Describe the morphology of the erythrocytes.
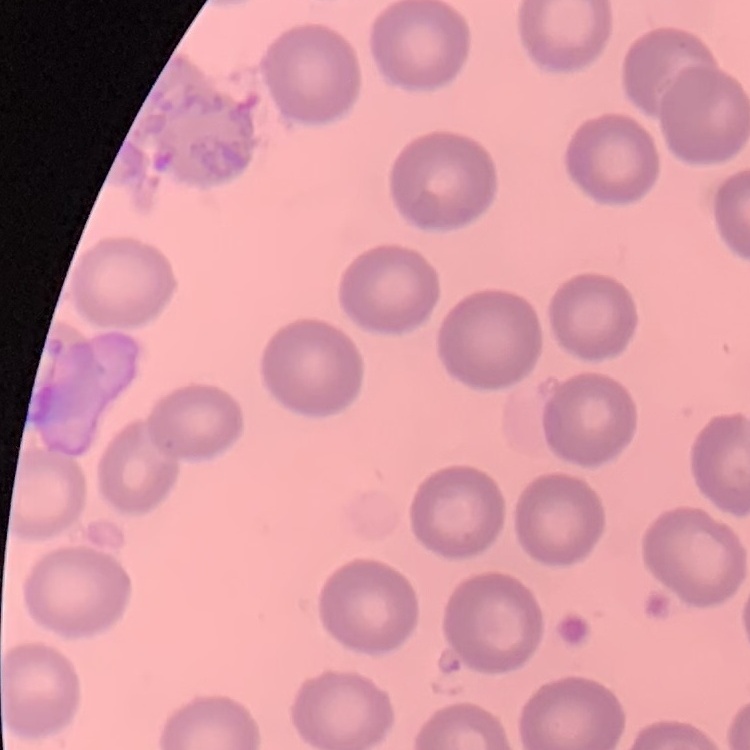

No rouleaux formation.

preparation = thin peripheral smear
image type = one tile cut from a larger photomicrograph
stain = Field's or Giemsa